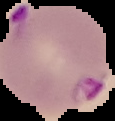
Summary:
  - Image size: 115×121 pixels
  - Image type: segmented cell region with the area outside set to black
  - Malaria status: parasitized
  - Preparation: thin blood smear